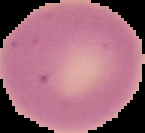

{
  "image_type": "cell region segmented out of the field of view; surrounding area masked to black",
  "image_size": "145×133 pixels",
  "malaria_status": "uninfected",
  "preparation": "thin blood smear"
}